Look for Plasmodium parasites.
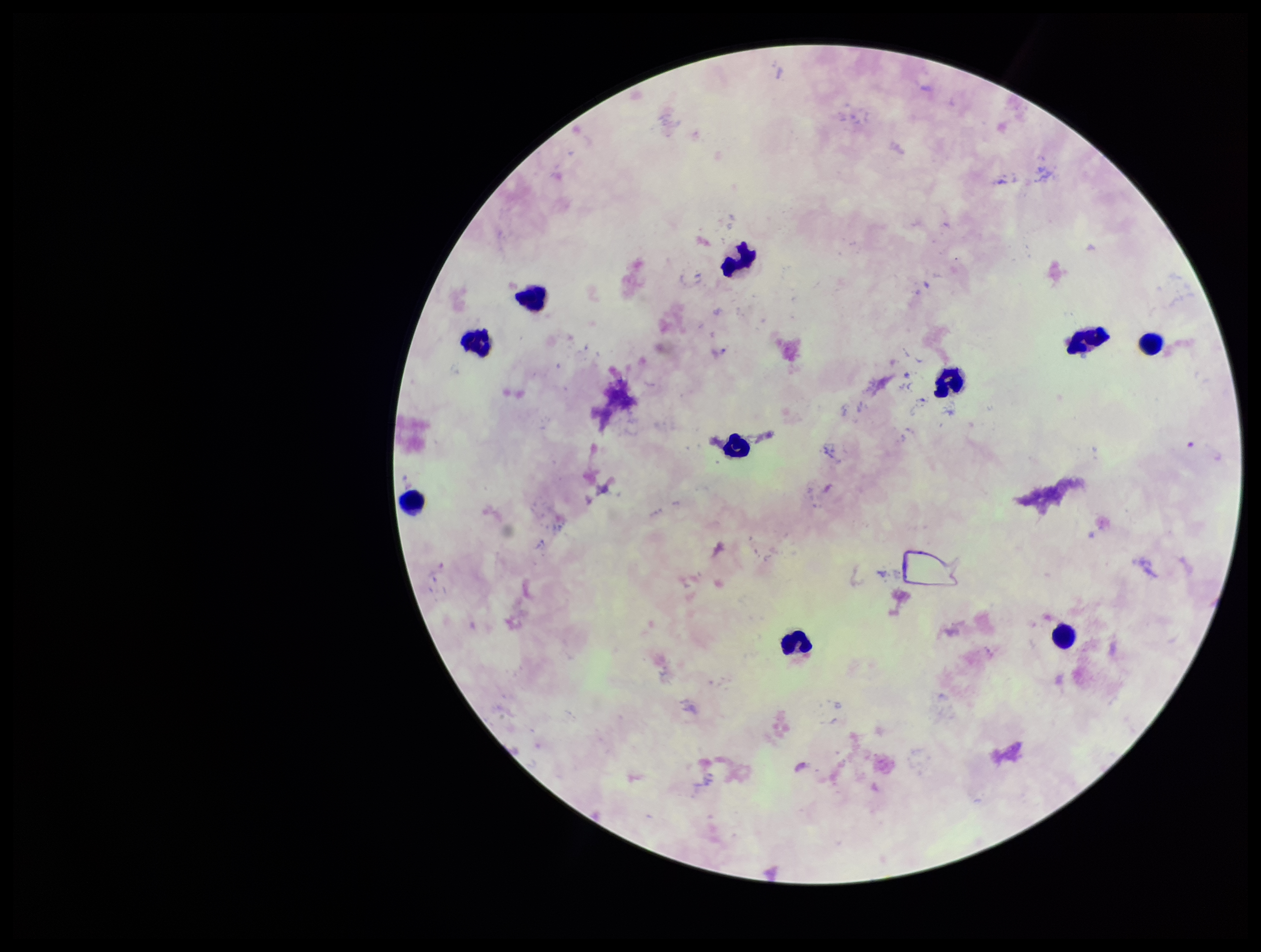

None detected.

Summary:
  - Parasite count: 0
  - Leukocyte count: 10
  - Capture: smartphone photograph through the microscope eyepiece
  - Patient malaria status: negative
  - Image size: 1261×952 pixels
  - Field of view: single
  - Preparation: thick blood smear
  - Stain: Giemsa